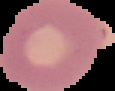 From a thin blood film. The area outside the segmented cell region is set to black. Image is 115×91 pixels. Malaria status: uninfected.